Locate every Trypanosoma brucei.
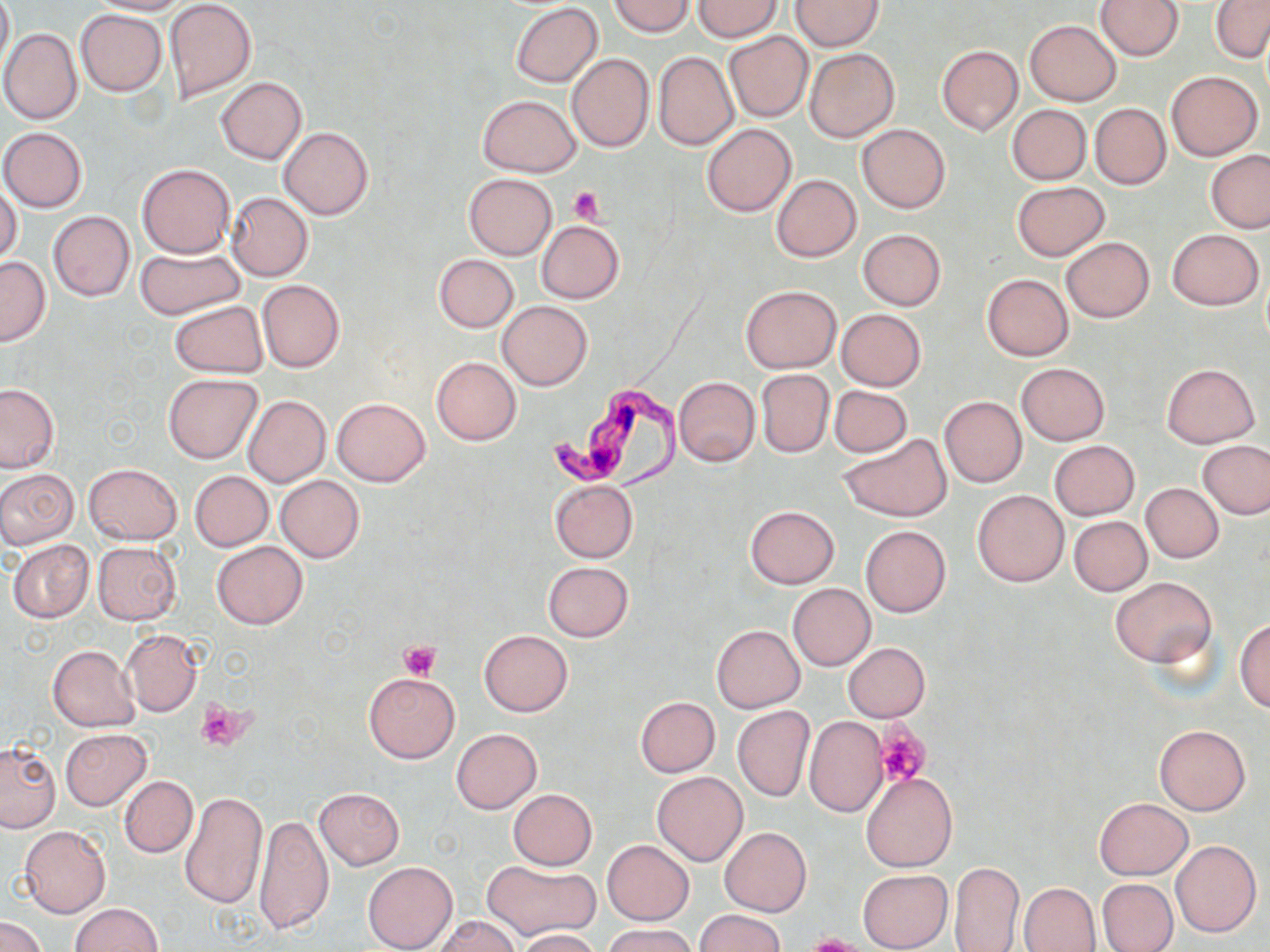

Approximate bounding boxes as [x1, y1, x2, y2] in pixels.
Trypanosoma brucei: [541, 374, 692, 497].

Summary:
  - Platelet locations: [567, 186, 608, 224], [398, 639, 442, 680], [197, 701, 248, 750], [875, 725, 928, 787], [803, 935, 866, 952]
  - Uninfected red blood cell locations: [0, 0, 13, 75], [85, 0, 189, 15], [163, 0, 256, 103], [609, 0, 694, 36], [792, 0, 884, 51], [1095, 0, 1183, 60], [693, 1, 781, 40], [1211, 2, 1270, 61], [511, 3, 603, 87], [75, 9, 167, 95], [1025, 19, 1122, 105], [1, 28, 82, 125], [724, 31, 813, 122], [936, 46, 1022, 135], [805, 48, 899, 142], [653, 50, 739, 151], [566, 52, 654, 152], [1166, 71, 1263, 160], [217, 77, 307, 163], [478, 95, 580, 175], [1090, 103, 1170, 189], [1008, 104, 1090, 185], [702, 124, 796, 217], [857, 124, 950, 214], [278, 127, 373, 219], [0, 128, 87, 213], [1206, 151, 1270, 233], [137, 162, 236, 258], [464, 173, 557, 260], [771, 175, 861, 262], [0, 181, 23, 266], [1012, 182, 1109, 260], [227, 192, 313, 280], [48, 211, 135, 302], [535, 220, 624, 304], [858, 229, 947, 310], [1167, 229, 1264, 310], [1059, 237, 1155, 323], [134, 246, 246, 319], [434, 254, 518, 333], [0, 257, 50, 346], [981, 274, 1073, 360], [257, 280, 345, 373], [740, 285, 842, 373], [497, 300, 592, 390], [170, 301, 267, 379], [835, 309, 927, 390], [432, 357, 521, 444], [1016, 362, 1110, 445], [1161, 363, 1260, 448], [755, 370, 835, 457], [163, 373, 263, 464], [674, 376, 760, 467], [0, 384, 58, 473], [829, 385, 912, 457], [243, 395, 330, 486], [938, 395, 1027, 488], [332, 398, 430, 486], [838, 432, 954, 522], [1049, 439, 1138, 520], [1199, 441, 1270, 518], [84, 463, 182, 544], [0, 469, 78, 549], [189, 470, 272, 551], [276, 475, 364, 563], [550, 480, 637, 562], [1141, 483, 1223, 563], [973, 490, 1068, 586], [744, 505, 839, 588], [1069, 516, 1152, 596], [860, 525, 950, 616], [7, 540, 93, 623], [92, 542, 181, 625], [211, 542, 307, 628], [543, 561, 633, 642], [1109, 577, 1216, 666], [788, 583, 874, 670], [1235, 618, 1270, 712], [710, 625, 805, 712], [121, 628, 203, 717], [479, 630, 572, 716], [843, 642, 930, 722], [47, 645, 140, 731], [363, 672, 459, 763], [635, 696, 720, 776], [733, 706, 814, 802], [805, 717, 888, 817], [1155, 724, 1250, 816], [451, 728, 541, 814], [60, 729, 152, 809], [0, 741, 60, 831], [862, 770, 957, 872], [652, 772, 747, 866], [119, 775, 197, 858], [314, 788, 404, 869], [508, 788, 596, 870], [180, 790, 266, 909], [1096, 797, 1191, 879], [254, 814, 335, 938], [19, 826, 110, 916], [720, 827, 811, 916], [602, 840, 694, 925], [1170, 840, 1261, 937], [481, 859, 600, 941], [949, 860, 1023, 952], [363, 861, 457, 951], [857, 868, 953, 952], [1097, 879, 1177, 952], [1018, 882, 1099, 951], [72, 903, 162, 952], [694, 910, 786, 952], [434, 914, 521, 952], [1, 916, 47, 952], [604, 923, 695, 952], [517, 929, 600, 952]
  - Slide-level diagnosis: Trypanosoma brucei
  - Image size: 1270×952 pixels
  - Magnification: 1000x
  - Modality: optical microscopy
  - Preparation: thin blood smear
  - Stain: May-Grünwald-Giemsa
  - Field of view: single